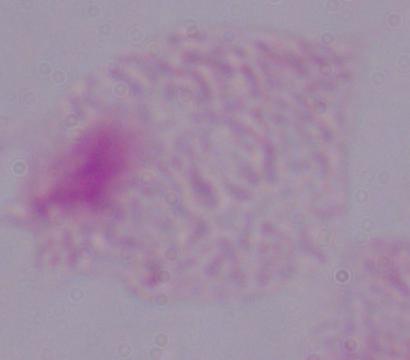

modality: photomicrograph
magnification: 1000x
identification: trichomonad